Assess this cell for malaria.
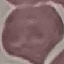
It is uninfected.

Summary:
  - Capture: smartphone camera at the microscope eyepiece
  - Image type: automatically extracted cell patch, resized to 64 × 64 pixels
  - Preparation: thin blood film
  - Stain: Giemsa